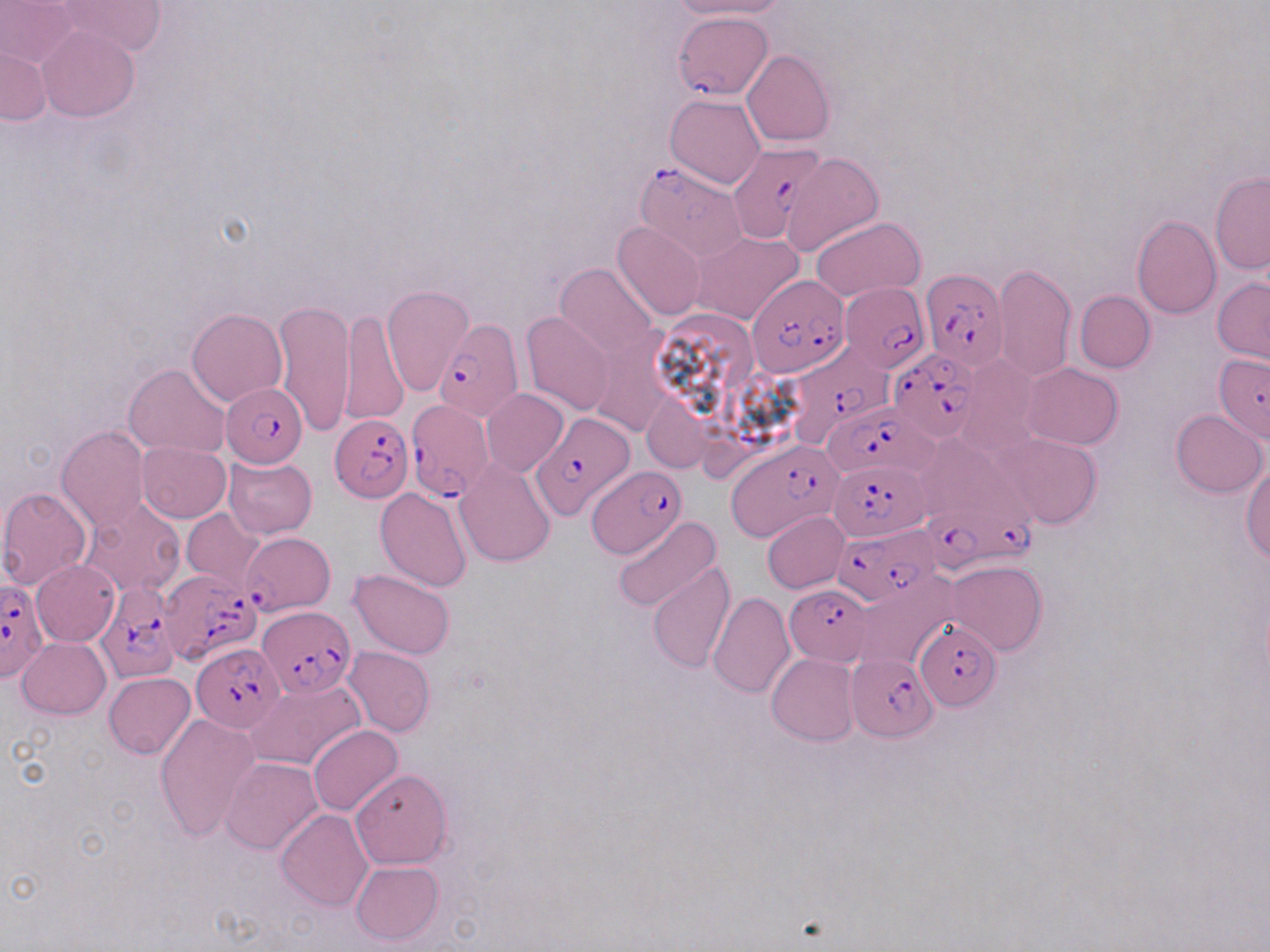
Plasmodium falciparum-infected red blood cell locations = approximate bounding boxes as (x1, y1, x2, y2) in pixels: (673, 14, 775, 99), (726, 142, 826, 241), (636, 162, 748, 261), (920, 267, 1005, 370), (747, 273, 851, 378), (840, 283, 930, 370), (434, 317, 521, 421), (888, 347, 980, 442), (793, 349, 900, 458), (221, 382, 309, 468), (407, 400, 495, 501), (825, 400, 935, 478), (528, 410, 634, 522), (331, 414, 412, 502), (728, 441, 842, 541), (830, 460, 930, 541), (587, 465, 686, 559), (914, 494, 1038, 572), (835, 524, 940, 601), (162, 568, 262, 682), (0, 579, 48, 684), (96, 582, 178, 686), (786, 584, 873, 665), (257, 607, 357, 698), (915, 622, 1002, 710), (192, 644, 284, 730), (846, 653, 939, 740)
slide-level diagnosis = Plasmodium falciparum
magnification = 1000x
modality = light microscopy
image size = 1270×952 pixels
preparation = thin blood smear
uninfected red blood cell locations = approximate bounding boxes as (x1, y1, x2, y2) in pixels: (0, 0, 81, 72), (663, 0, 786, 20), (55, 1, 167, 57), (38, 25, 139, 122), (2, 48, 51, 126), (741, 50, 835, 147), (665, 93, 766, 188), (781, 152, 884, 255), (1210, 170, 1270, 275), (1130, 214, 1221, 318), (810, 215, 924, 302), (612, 222, 706, 322), (694, 231, 802, 326), (556, 263, 659, 361), (994, 264, 1076, 382), (1212, 277, 1270, 365), (382, 284, 474, 398), (1075, 290, 1155, 372), (273, 299, 356, 438), (339, 307, 407, 427), (187, 308, 288, 407), (521, 311, 615, 416), (1214, 353, 1270, 441), (956, 355, 1042, 455), (1022, 363, 1123, 449), (124, 364, 230, 459), (482, 389, 569, 477), (644, 397, 710, 472), (1170, 409, 1267, 498), (57, 426, 149, 531), (989, 432, 1104, 529), (138, 442, 231, 523), (222, 454, 318, 539), (454, 457, 556, 567), (1241, 460, 1270, 562), (384, 474, 547, 580), (0, 487, 92, 589), (374, 487, 473, 593), (81, 497, 187, 599), (181, 509, 265, 591), (762, 510, 848, 593), (613, 518, 721, 614), (243, 532, 335, 615), (32, 560, 119, 647), (946, 560, 1046, 655), (648, 562, 737, 670), (348, 569, 455, 659), (853, 571, 960, 673), (708, 591, 795, 699), (18, 637, 110, 719), (343, 646, 435, 735), (768, 653, 860, 745), (104, 672, 195, 759), (246, 679, 366, 772), (155, 713, 260, 842), (308, 724, 403, 816), (221, 757, 322, 854), (351, 769, 451, 869), (277, 810, 374, 912), (350, 861, 443, 946)
stain = May-Grünwald-Giemsa
field of view = single